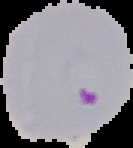 Image is 133×148 pixels. Cell region segmented out of the field of view; the surrounding area is masked to black. Malaria status: parasitized. From a thin blood smear.